Assess the morphology of the erythrocytes.
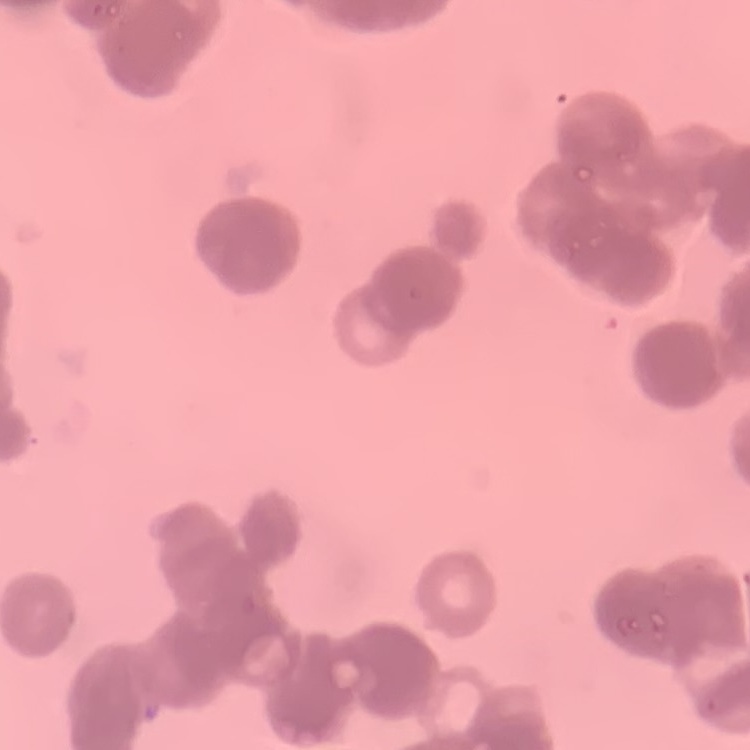

Rouleaux formation.

Thin peripheral smear. Stained with either Field's or Giemsa. One tile cut from a larger photomicrograph.